Report the malaria status of this cell.
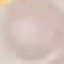

It is uninfected.

Cell patch, automatically extracted from a larger field of view and resized to 64 × 64 pixels. Thin blood film. Acquired by smartphone through the microscope eyepiece. Giemsa stain.